Assess this cell for malaria.
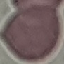
It is uninfected.

{
  "image_type": "automatically extracted cell patch, resized to 64 × 64 pixels",
  "capture": "smartphone through the microscope eyepiece",
  "stain": "Giemsa",
  "preparation": "thin smear"
}